Give the extent of all Plasmodium falciparum-infected red blood cells.
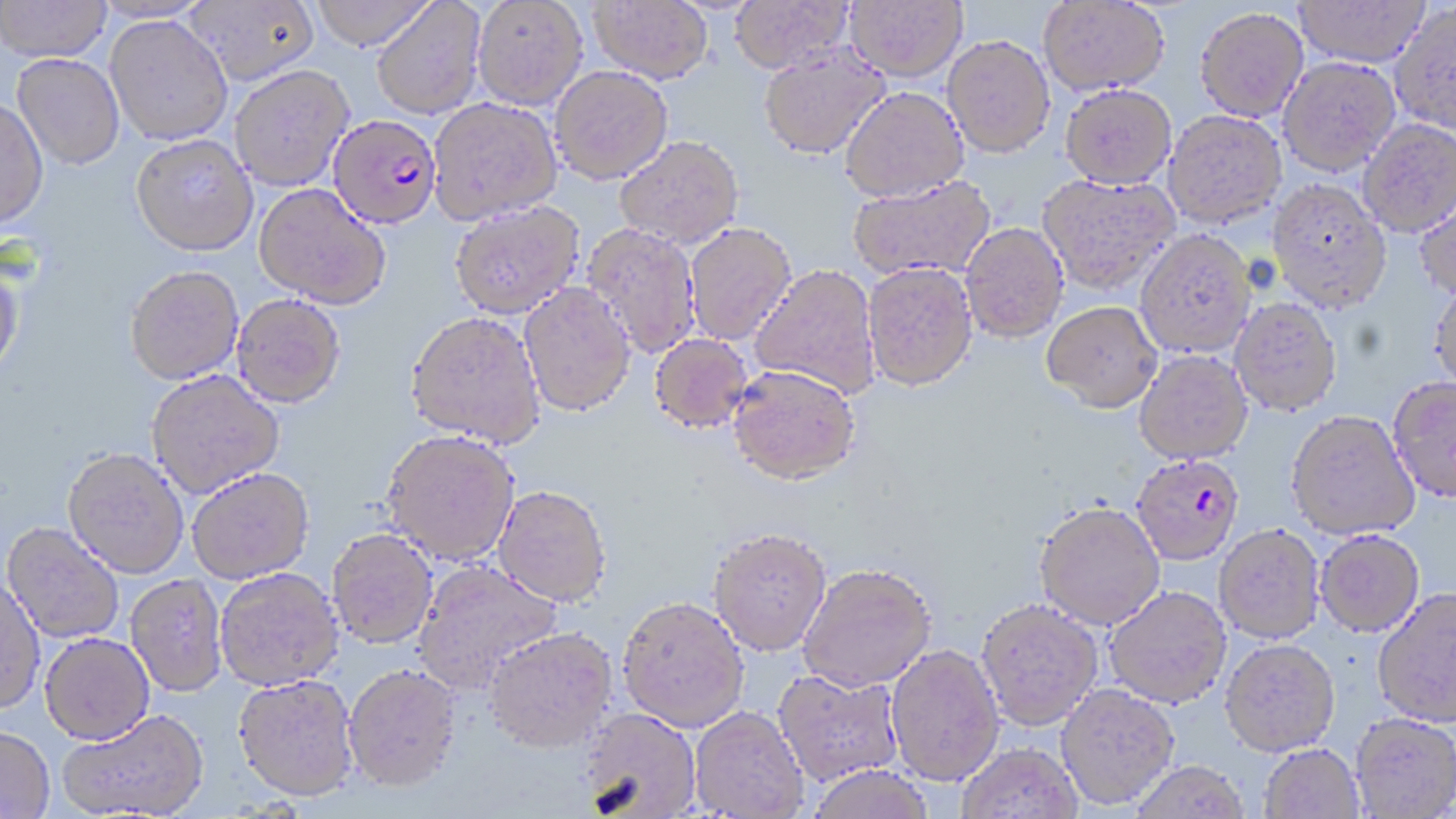

Approximate bounding boxes as (x1,y1)-(x2,y2) corner pairs in pixels.
Plasmodium falciparum-infected red blood cells: (328,114)-(443,228), (1131,453)-(1245,564).

Summary:
  - Uninfected red blood cell locations: (0,0)-(112,61), (185,0)-(319,86), (308,0)-(437,50), (472,0)-(588,110), (729,0)-(854,74), (845,0)-(967,81), (1038,0)-(1170,95), (371,1)-(487,120), (589,1)-(714,85), (1294,1)-(1430,68), (1390,3)-(1456,135), (1195,7)-(1308,122), (105,14)-(233,145), (943,34)-(1055,157), (758,44)-(889,160), (12,54)-(124,169), (1278,56)-(1400,175), (229,64)-(354,191), (549,65)-(673,184), (1060,84)-(1177,189), (840,86)-(969,202), (0,98)-(49,231), (428,98)-(563,224), (1163,110)-(1286,229), (1358,119)-(1456,236), (130,134)-(258,257), (614,135)-(743,249), (1037,172)-(1179,295), (848,176)-(996,280), (1266,178)-(1391,313), (254,183)-(390,309), (1414,192)-(1456,301), (449,199)-(585,318), (684,222)-(797,346), (960,222)-(1068,343), (582,223)-(702,358), (1135,229)-(1257,358), (862,261)-(978,391), (0,263)-(24,379), (749,264)-(881,399), (125,265)-(244,384), (1427,278)-(1456,393), (519,282)-(636,417), (232,294)-(346,408), (1229,298)-(1342,417), (1042,300)-(1162,412), (406,311)-(546,448), (649,333)-(753,433), (1134,350)-(1253,464), (727,364)-(861,485), (146,369)-(284,499), (1387,377)-(1456,505), (1286,410)-(1420,541), (381,429)-(520,565), (63,449)-(188,579), (187,468)-(314,584), (493,485)-(611,607), (1034,502)-(1165,630), (2,523)-(124,644), (1214,524)-(1325,644), (709,526)-(831,656), (327,528)-(438,649), (1315,530)-(1425,638), (412,560)-(563,695), (797,563)-(936,692), (215,568)-(343,691), (0,572)-(46,716), (125,574)-(228,698), (1104,587)-(1232,710), (1373,588)-(1456,729), (617,596)-(750,733), (976,599)-(1104,731), (485,628)-(617,754), (39,634)-(155,746), (1219,640)-(1341,759), (885,644)-(1004,788), (344,665)-(462,794), (773,669)-(904,787), (232,675)-(360,803), (1056,685)-(1179,811), (690,707)-(809,818), (579,708)-(702,818), (58,709)-(210,818), (1350,715)-(1456,818), (0,727)-(55,818), (956,743)-(1083,819), (1258,745)-(1364,819), (1130,762)-(1251,818), (807,766)-(934,819)
  - Slide-level diagnosis: Plasmodium falciparum
  - Magnification: 1000x
  - Modality: optical microscopy
  - Preparation: thin blood film
  - Image size: 1456×819 pixels
  - Field of view: one of a larger specimen
  - Stain: May-Grünwald-Giemsa